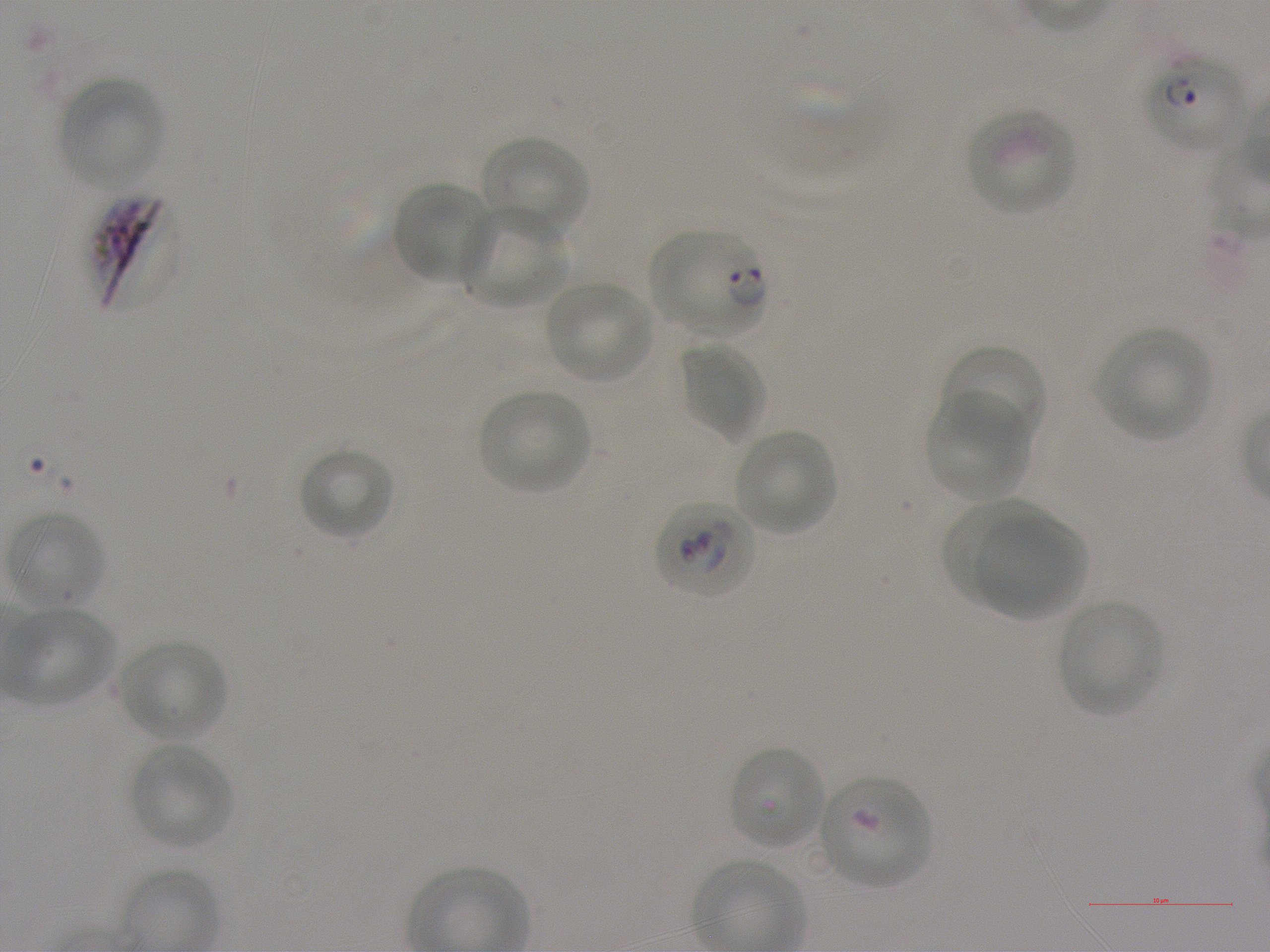
Not every red blood cell is marked. A life-cycle stage — or a range of stages, where the recorded stages span more than one — follows each staged infected red blood cell.
donor blood group = A+
field of view = single
locations of red blood cells of indeterminate infection status = approximate bounding boxes as {x1, y1, x2, y2} in pixels: {651, 498, 760, 600}, {729, 745, 825, 850}, {819, 774, 931, 887}
locations of infected red blood cells = approximate bounding boxes as {x1, y1, x2, y2} in pixels: {1146, 50, 1248, 152} ring; {88, 187, 172, 314}; {651, 228, 767, 336} ring
stain = Giemsa
objective = 100x, oil immersion, numerical aperture 1.25
image size = 1270×952 pixels
culture = Plasmodium falciparum strain NF54, static, in vitro
locations of uninfected red blood cells = approximate bounding boxes as {x1, y1, x2, y2} in pixels: {57, 76, 164, 188}, {964, 107, 1077, 217}, {482, 135, 588, 239}, {391, 181, 494, 285}, {458, 207, 571, 311}, {546, 280, 654, 384}, {1097, 327, 1212, 439}, {678, 341, 767, 443}, {941, 344, 1048, 451}, {478, 388, 593, 495}, {926, 389, 1031, 499}, {734, 430, 835, 536}, {297, 446, 394, 541}, {938, 496, 1068, 599}, {6, 511, 105, 610}, {976, 517, 1084, 618}, {1057, 600, 1164, 716}, {5, 607, 118, 707}, {120, 641, 226, 743}, {130, 745, 233, 849}, {695, 859, 801, 943}
preparation = thin blood smear